Point out each Plasmodium parasite and each leukocyte.
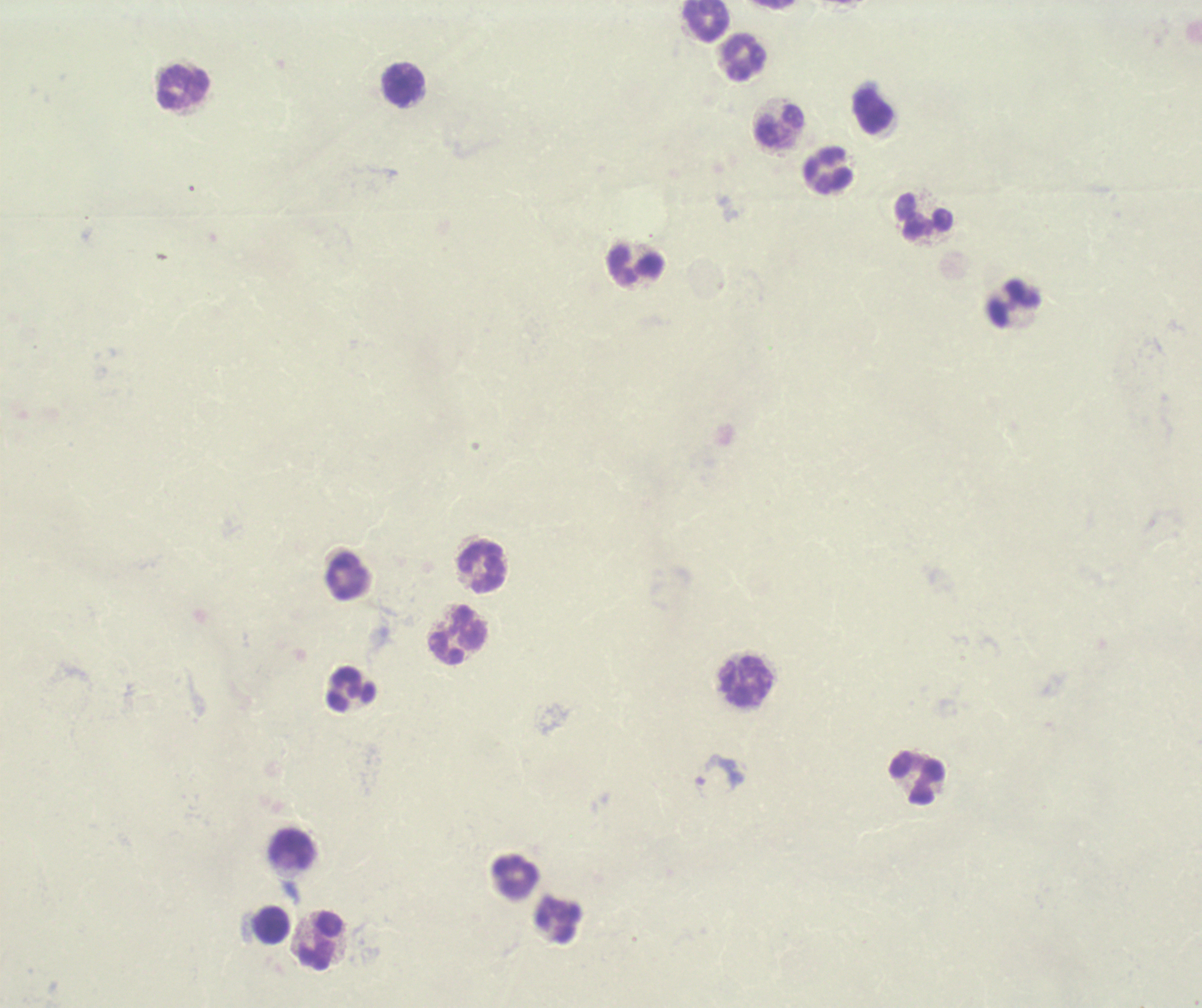

Negative for Plasmodium parasites.
Approximate centers as {x, y} in pixels.
Leukocytes: {706, 20}, {743, 57}, {402, 86}, {184, 88}, {872, 111}, {780, 126}, {829, 170}, {924, 218}, {635, 267}, {1014, 303}, {483, 567}, {347, 576}, {457, 634}, {746, 681}, {350, 689}, {917, 778}, {293, 850}, {516, 878}, {558, 920}, {271, 925}, {321, 942}.

Image is 1202×1008 pixels. Previously used in an actual diagnosis. Captured at 100x magnification. Romanowsky stain. Thick blood smear. Single field of view. Background quality: poor.